State which cell type is depicted.
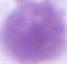

An erythrocyte.

{
  "magnification": "1000x",
  "modality": "micrograph"
}